Name the blood parasite species.
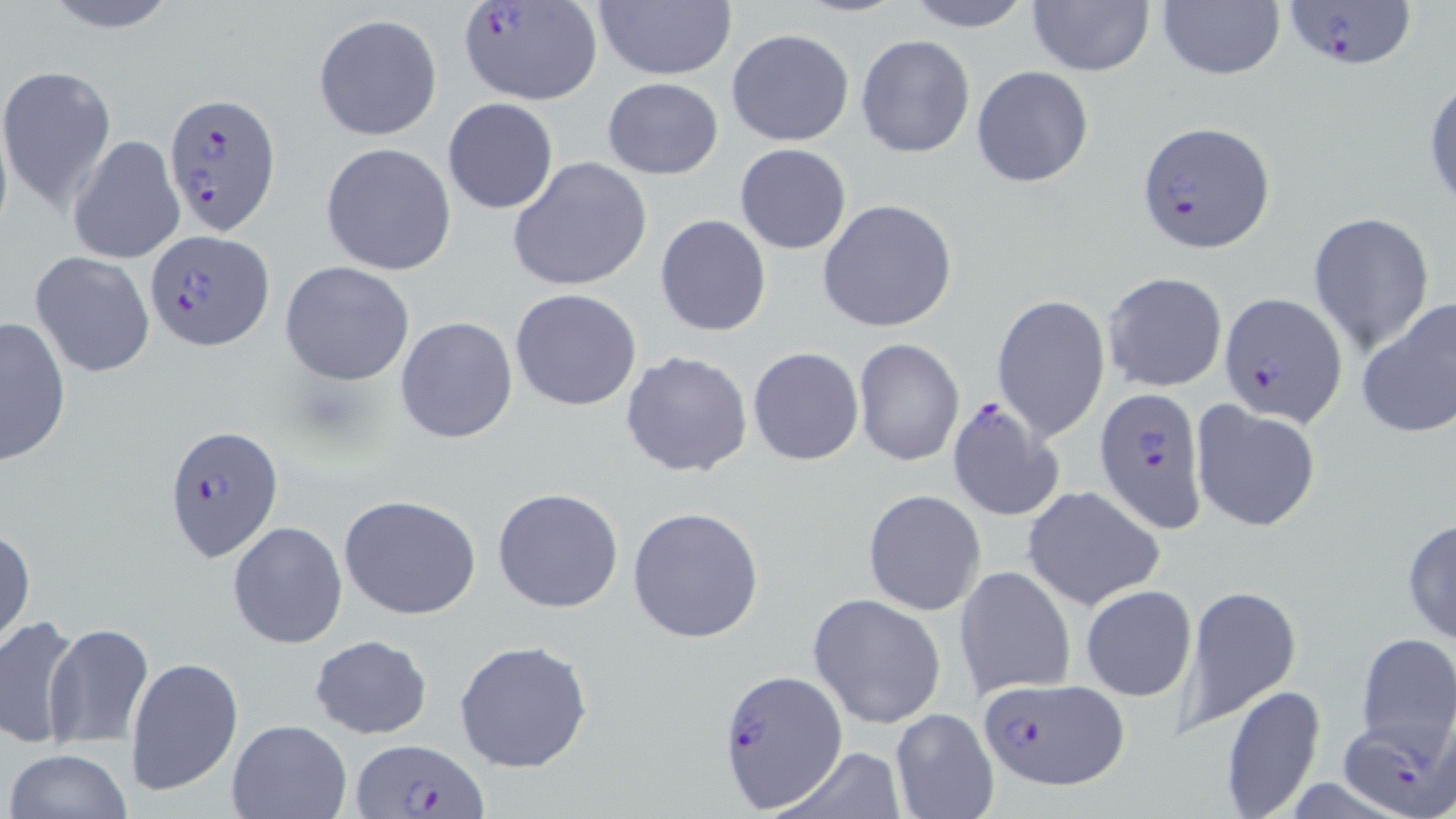

Plasmodium falciparum.

Summary:
  - Coordinate format: approximate bounding boxes as [x1, y1, x2, y2] in pixels
  - Plasmodium falciparum-infected red blood cell locations: [459, 0, 603, 106], [1283, 0, 1420, 70], [163, 91, 280, 232], [1137, 120, 1275, 254], [144, 229, 273, 351], [1221, 293, 1346, 427], [1095, 387, 1207, 531], [945, 397, 1063, 523], [163, 423, 285, 564], [719, 670, 850, 813], [974, 677, 1127, 789], [1339, 717, 1456, 819], [353, 737, 486, 819]
  - Uninfected red blood cell locations: [33, 0, 185, 33], [900, 0, 1038, 31], [1027, 0, 1153, 75], [592, 1, 736, 81], [1157, 2, 1285, 81], [312, 14, 442, 140], [726, 28, 855, 146], [856, 34, 975, 159], [971, 64, 1095, 188], [0, 66, 121, 213], [1424, 75, 1456, 210], [601, 77, 725, 178], [442, 97, 559, 214], [67, 134, 186, 265], [320, 142, 458, 275], [735, 143, 852, 254], [507, 155, 653, 293], [816, 199, 957, 333], [1309, 213, 1436, 352], [654, 214, 773, 338], [31, 251, 155, 379], [280, 261, 416, 385], [1102, 271, 1228, 393], [510, 289, 642, 410], [992, 293, 1108, 442], [1356, 298, 1456, 441], [395, 315, 520, 444], [1, 316, 72, 465], [852, 337, 964, 468], [748, 347, 864, 465], [620, 350, 753, 479], [1192, 402, 1322, 532], [1022, 485, 1165, 610], [493, 488, 623, 613], [863, 489, 986, 614], [337, 493, 483, 621], [626, 506, 767, 644], [1402, 516, 1456, 646], [227, 520, 347, 651], [1, 524, 35, 655], [954, 566, 1076, 701], [1080, 584, 1197, 703], [1180, 584, 1301, 730], [809, 593, 946, 729], [0, 614, 85, 750], [44, 622, 154, 747], [1353, 631, 1456, 762], [308, 634, 433, 740], [453, 639, 594, 774], [126, 656, 243, 799], [1218, 683, 1327, 817], [889, 708, 999, 819], [226, 719, 351, 819], [768, 745, 911, 819], [4, 748, 134, 819]
  - Modality: light microscopy
  - Image size: 1456×819 pixels
  - Stain: May-Grünwald-Giemsa
  - Magnification: 1000x
  - Field of view: one of a larger specimen
  - Preparation: thin blood smear